Classify the preparation.
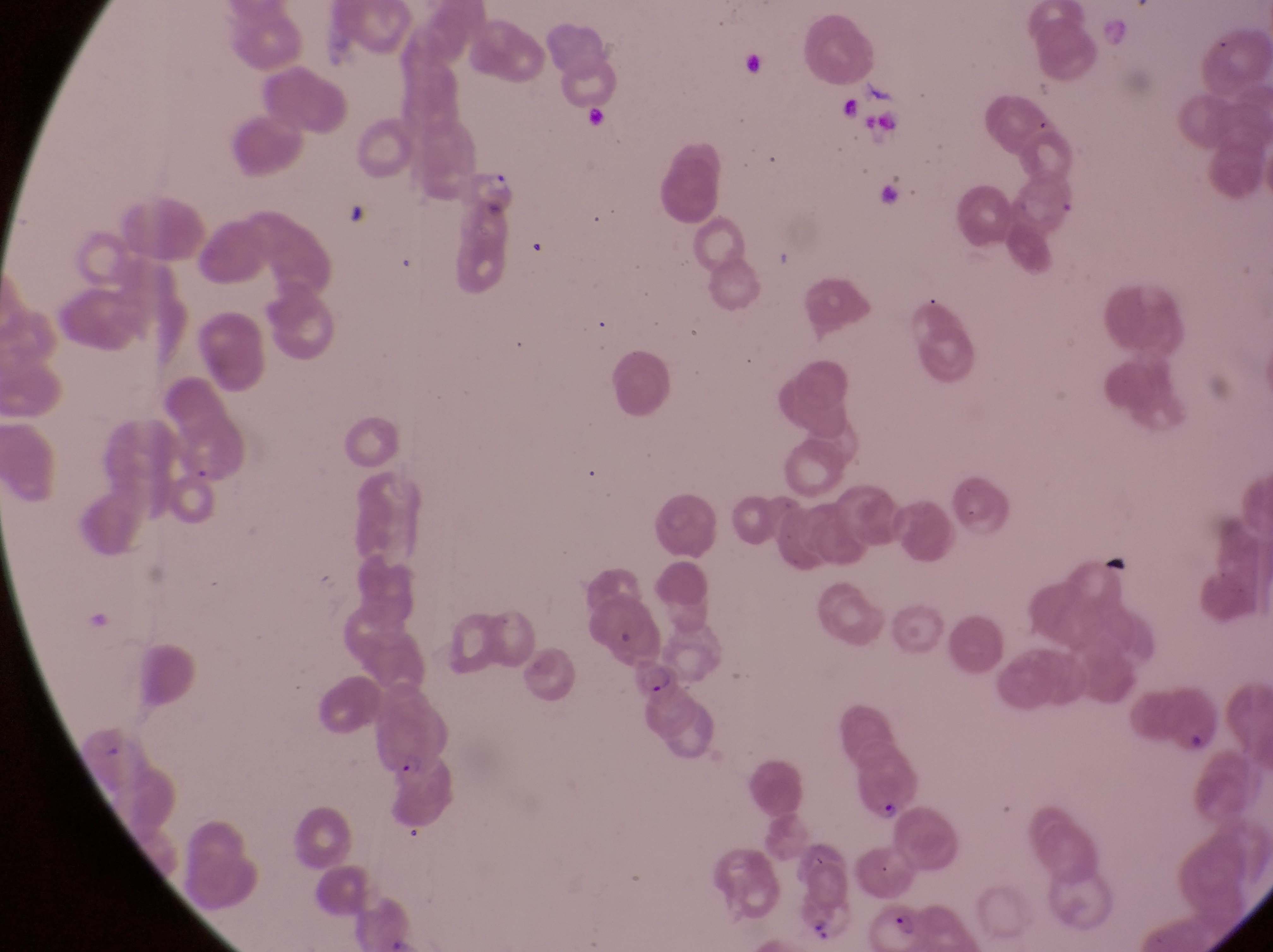

Thin blood film.

Approximate bounding boxes as left top right bottom in pixels. Artifact (platelet-like body, stain precipitate, or debris) locations: 841 92 863 125. Parasitised red blood cell locations: 624 657 684 710; 851 757 928 834; 878 894 926 947. Trophozoite locations: 484 164 519 196; 384 749 429 784. One field of view. At a magnification of 1000x. Sample from Uganda. Photographed through the eyepiece of an Olympus CX-23 microscope with a smartphone camera. Image is 1273×952 pixels.